Comment on the morphology of the red blood cells.
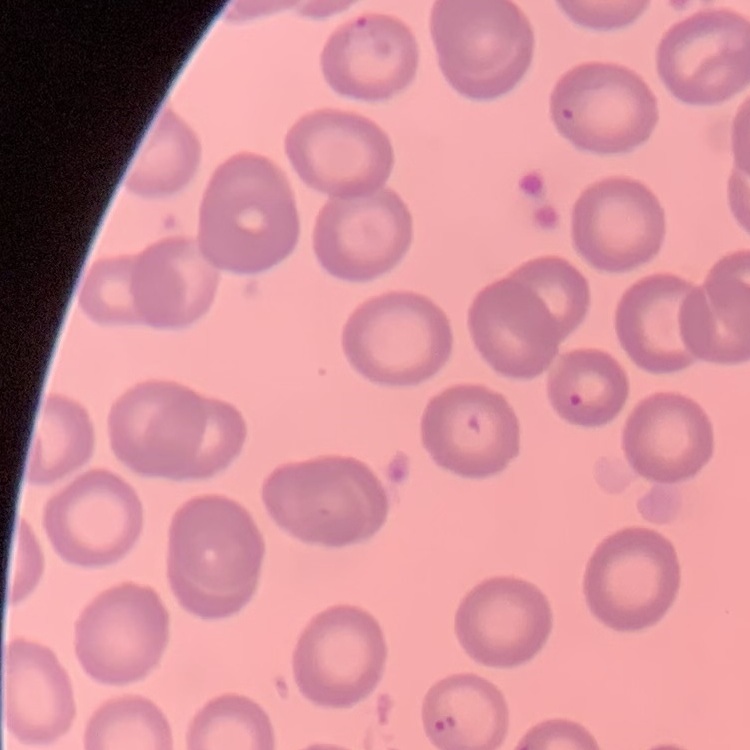
No rouleaux formation.

{
  "stain": "Field's or Giemsa",
  "image_type": "square crop of a larger photomicrograph",
  "preparation": "thin peripheral smear"
}